Report the malaria status of this cell.
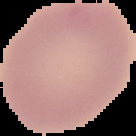

Uninfected.

image type = cell region segmented out of the field of view; surrounding area masked to black
image size = 136×136 pixels
preparation = thin blood smear